Point out Plasmodium parasites and leukocytes.
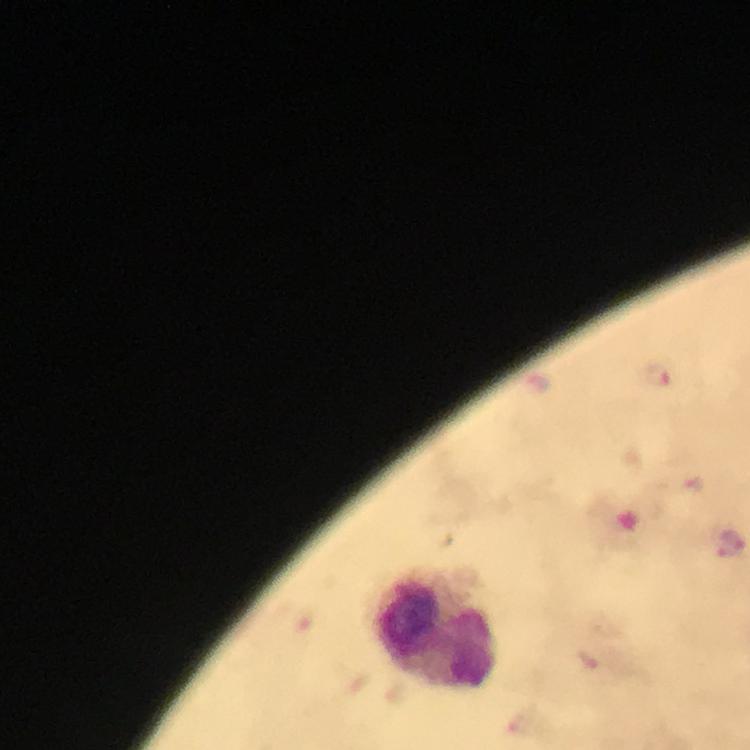

Approximate centers as [x, y] in pixels.
Plasmodium parasites: [659, 377], [732, 545].
Leukocytes: [437, 634].

Summary:
  - Stain: Giemsa
  - Context: from a diagnostic examination for malaria
  - Capture: smartphone camera through the microscope
  - Image size: 750×750 pixels
  - Cropped from: one field of view
  - Magnification: 100x
  - Immersion oil: applied
  - Preparation: thick blood film